Describe the morphology of the red blood cells.
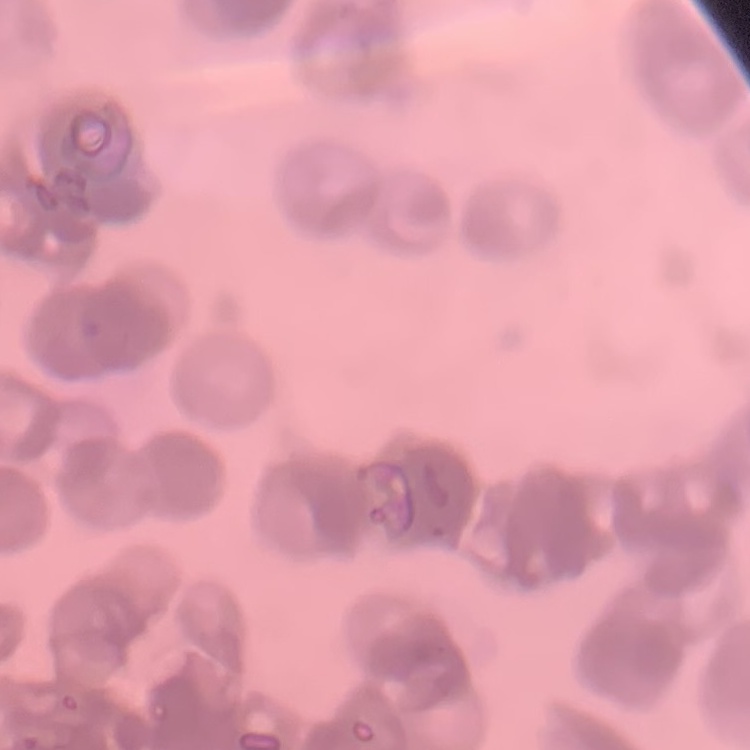
They show rouleaux formation.

One tile cut from a larger photomicrograph. Thin blood film. Field's or Giemsa stain.